Point out each malaria parasite.
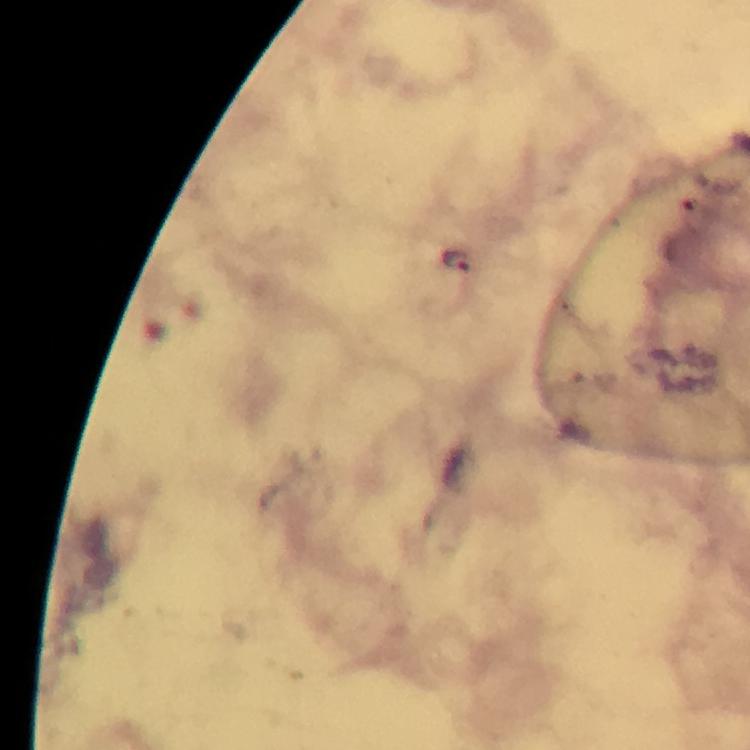

Approximate centers as (x, y) in pixels.
Malaria parasites: (457, 260).

Summary:
  - Context: from a diagnostic examination for malaria
  - Capture: smartphone mounted on the microscope
  - Stain: Giemsa
  - Image size: 750×750 pixels
  - Immersion oil: used
  - Magnification: 100x
  - Preparation: thick blood smear
  - Cropped from: a single field of view